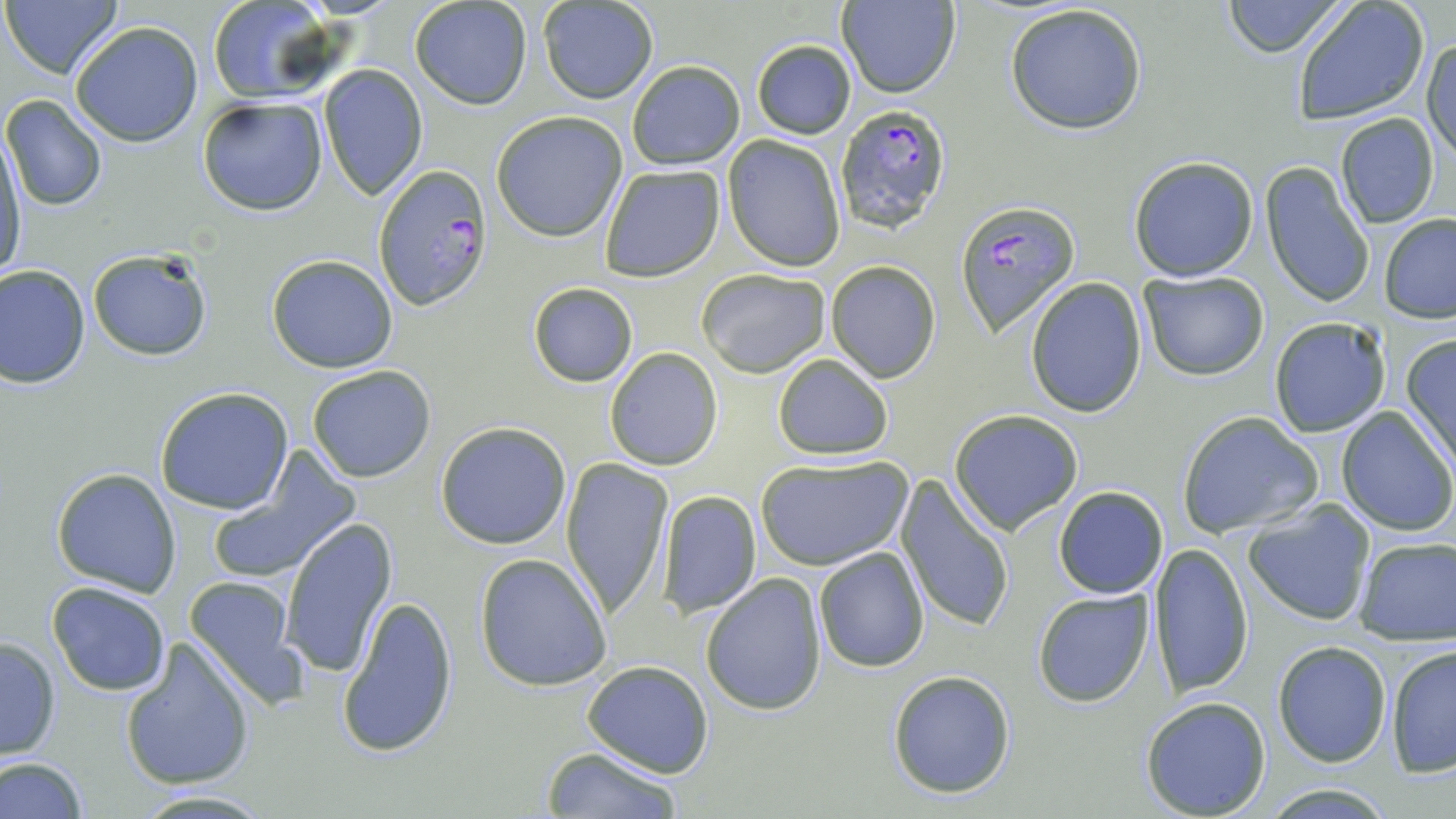

slide-level diagnosis = Plasmodium falciparum
modality = light microscopy
Plasmodium falciparum-infected red blood cell locations = approximate bounding boxes as (x1, y1, x2, y2) in pixels: (834, 104, 951, 234), (372, 164, 492, 309), (953, 199, 1081, 337)
preparation = thin blood film
magnification = 1000x
field of view = single
stain = May-Grünwald-Giemsa
uninfected red blood cell locations = approximate bounding boxes as (x1, y1, x2, y2) in pixels: (4, 0, 122, 79), (207, 0, 332, 101), (837, 0, 961, 98), (1221, 0, 1349, 57), (409, 1, 531, 110), (538, 1, 658, 103), (1290, 1, 1431, 124), (1004, 3, 1149, 135), (70, 21, 204, 148), (1423, 35, 1456, 162), (751, 38, 856, 139), (626, 61, 744, 169), (317, 66, 427, 199), (2, 95, 106, 212), (196, 97, 328, 216), (491, 111, 628, 241), (1334, 113, 1441, 228), (1, 129, 26, 281), (722, 135, 846, 272), (1126, 155, 1259, 282), (598, 162, 725, 282), (1260, 162, 1375, 308), (1379, 215, 1456, 322), (86, 246, 214, 362), (266, 254, 400, 373), (824, 260, 941, 384), (0, 263, 91, 388), (696, 267, 831, 378), (1138, 271, 1270, 382), (1025, 279, 1148, 417), (527, 281, 638, 386), (1268, 316, 1392, 437), (1400, 335, 1456, 469), (604, 348, 724, 469), (771, 353, 894, 459), (306, 365, 437, 481), (155, 387, 295, 516), (1336, 406, 1454, 535), (949, 409, 1084, 535), (1175, 411, 1323, 539), (435, 420, 572, 549), (754, 453, 913, 572), (207, 454, 360, 584), (560, 455, 676, 620), (51, 466, 182, 598), (896, 476, 1016, 634), (1053, 486, 1169, 599), (658, 491, 762, 616), (1243, 500, 1376, 627), (278, 517, 398, 677), (1353, 537, 1456, 642), (1147, 542, 1255, 697), (813, 548, 930, 673), (474, 553, 613, 691), (700, 572, 828, 717), (184, 573, 306, 700), (45, 581, 172, 696), (1032, 588, 1155, 708), (336, 593, 461, 757), (0, 636, 61, 760), (119, 638, 256, 792), (1273, 640, 1392, 767), (1384, 645, 1456, 776), (581, 659, 715, 776), (887, 670, 1016, 798), (1140, 695, 1271, 818), (541, 745, 683, 819), (0, 757, 87, 818), (129, 789, 278, 817)
image size = 1456×819 pixels